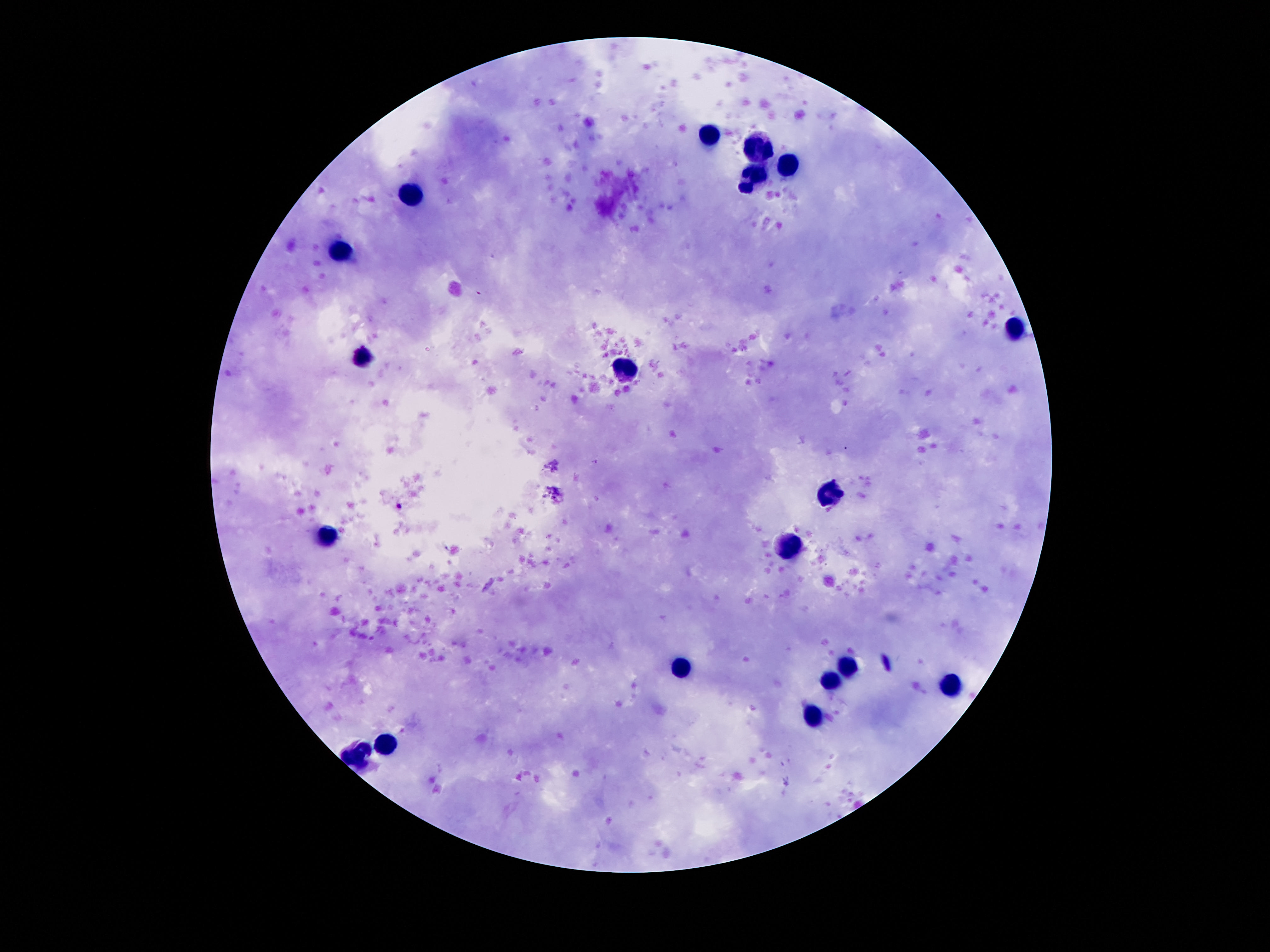
{
  "image_size": "1270×952 pixels",
  "preparation": "thick blood smear",
  "stain": "Giemsa",
  "leukocyte_locations": "approximate centers as {x, y} in pixels: {706, 135}, {755, 147}, {788, 166}, {751, 178}, {413, 192}, {337, 251}, {1014, 330}, {362, 356}, {622, 367}, {829, 489}, {325, 538}, {790, 545}, {850, 666}, {675, 668}, {831, 679}, {950, 684}, {811, 717}, {391, 743}, {356, 756}",
  "magnification": "100x",
  "field_of_view": "single",
  "patient_malaria_status": "not infected",
  "capture": "smartphone camera through the microscope eyepiece"
}